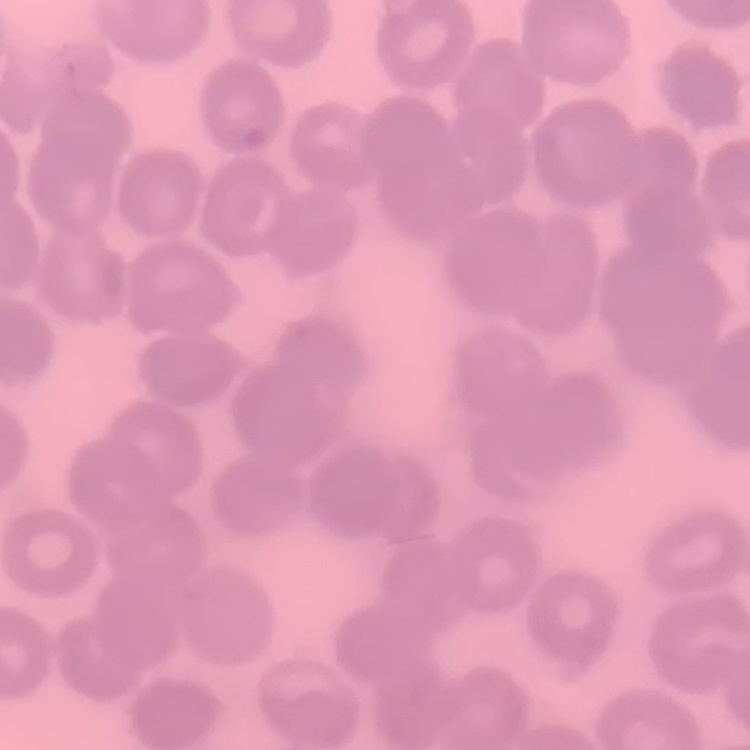 The erythrocytes exhibit no rouleaux formation. One tile cut from a larger photomicrograph. Field's or Giemsa stain. Thin blood film.